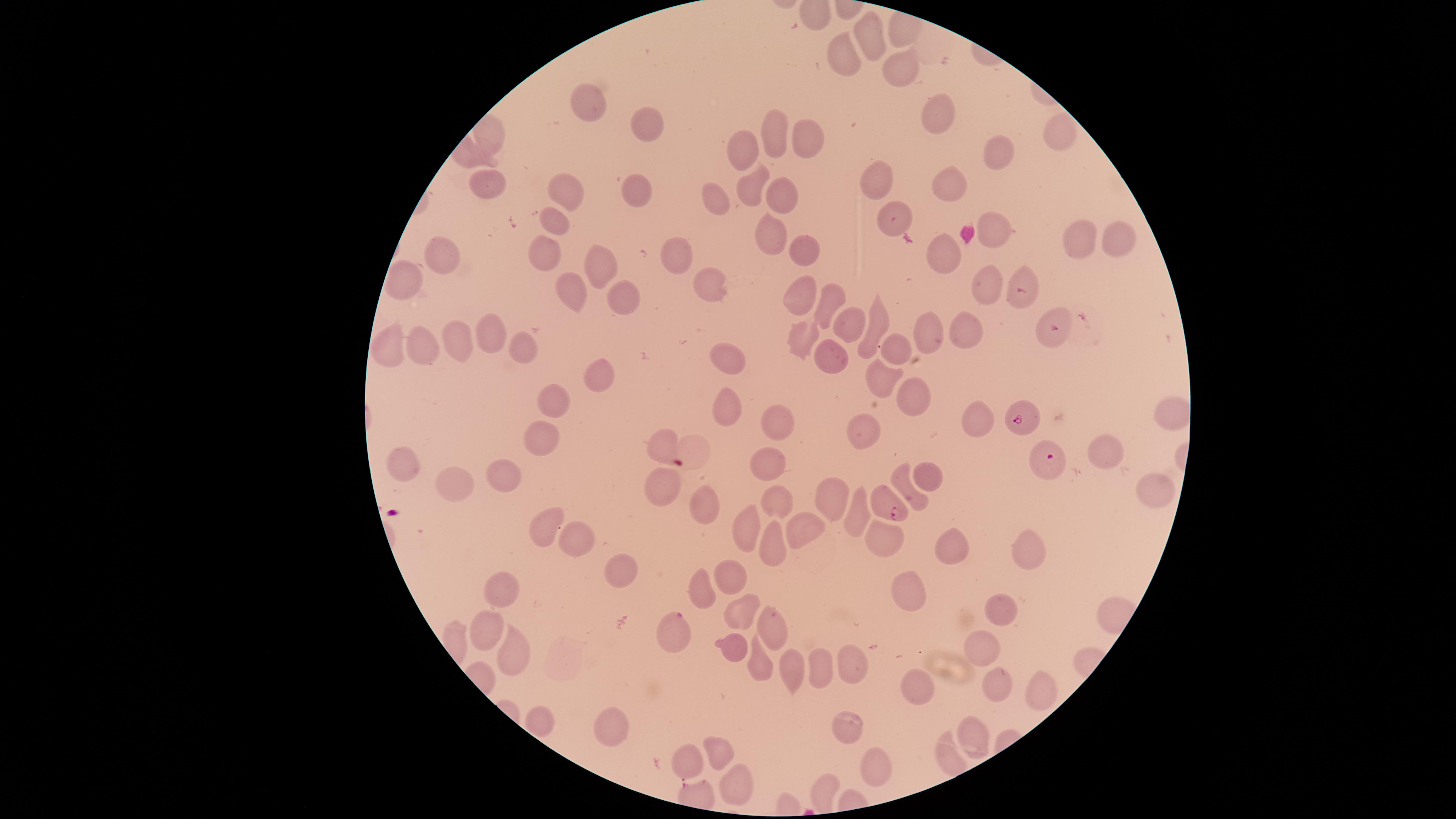
stain: Giemsa
visible_region: circular
field_of_view: single
capture: smartphone photograph through the microscope eyepiece
image_size: 1456×819 pixels
species: Plasmodium falciparum
presence: malaria parasites detected
preparation: thin smear of blood
uninfected_red_blood_cells: 'approximate marker points as [x, y] in pixels: [867, 41], [844, 58], [900, 74], [587, 105], [934, 118], [644, 122], [772, 130], [1062, 132], [489, 135], [808, 143], [749, 153], [1003, 154], [882, 182], [751, 184], [485, 185], [937, 185], [636, 188], [779, 189], [570, 190], [718, 196], [894, 220], [554, 223], [993, 231], [768, 232], [1119, 239], [1078, 242], [801, 249], [673, 252], [541, 254], [941, 254], [439, 256], [595, 265], [1022, 278], [704, 281], [404, 284], [987, 288], [570, 294], [800, 295], [624, 300], [828, 301], [843, 324], [876, 326], [964, 326], [926, 331], [1047, 331], [494, 332], [458, 337], [794, 340], [422, 347], [520, 350], [387, 351], [726, 352], [890, 353], [829, 355], [598, 377], [884, 380], [909, 396], [555, 401], [727, 406], [1167, 415], [980, 416], [778, 424], [860, 429], [540, 439], [656, 445], [1107, 457], [401, 460], [767, 461], [925, 473], [502, 479], [902, 484], [455, 485], [1154, 485], [663, 495], [696, 499], [773, 499], [825, 502], [854, 516], [750, 525], [551, 527], [801, 529], [578, 537], [771, 542], [884, 543], [945, 545], [1030, 550], [626, 568], [726, 576], [698, 586], [504, 587], [906, 591], [1000, 609], [735, 619], [766, 628], [489, 630], [988, 645], [735, 651], [519, 652], [821, 666], [759, 669], [849, 670], [791, 672], [999, 682], [915, 688], [1037, 691], [537, 718], [842, 725], [613, 727], [969, 733], [716, 751], [687, 762], [872, 767], [820, 786], [732, 787]'
parasitized_red_blood_cells: 'approximate marker points as [x, y] in pixels: [1023, 422], [1052, 461], [888, 510], [672, 633]'